Identify the parasite.
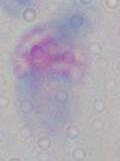

This is Toxoplasma gondii.

magnification = 1000x
modality = micrograph